Give the preparation type.
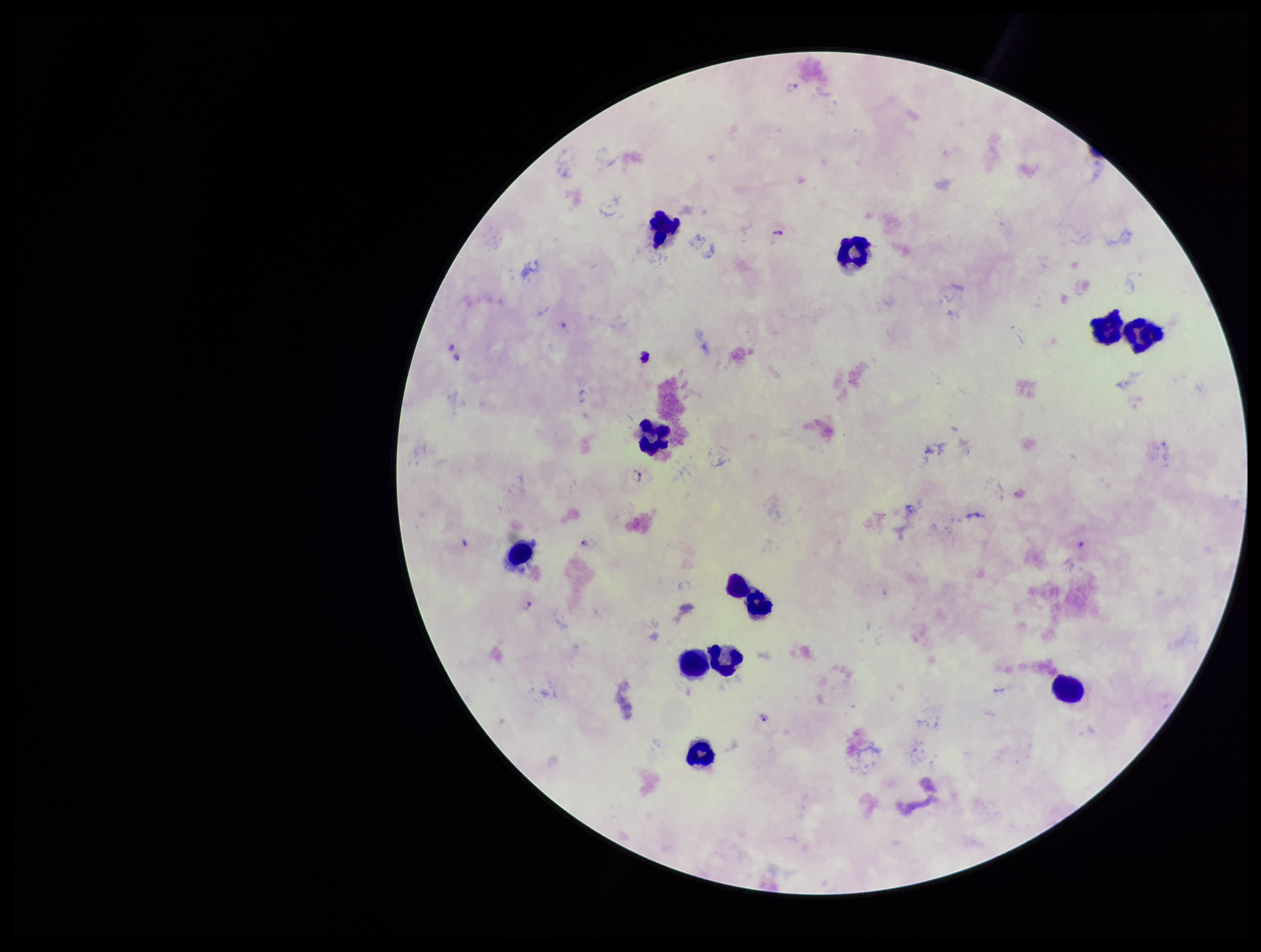
A thick smear.

Summary:
  - Stain: Giemsa
  - Plasmodium parasites: seen
  - Species reported for this patient: Plasmodium falciparum
  - Field of view: single
  - Leukocyte count: 12
  - Capture: smartphone photograph through the microscope eyepiece
  - Image size: 1261×952 pixels
  - Parasite count: 9
  - Patient malaria status: infected